Give the position of every malaria parasite.
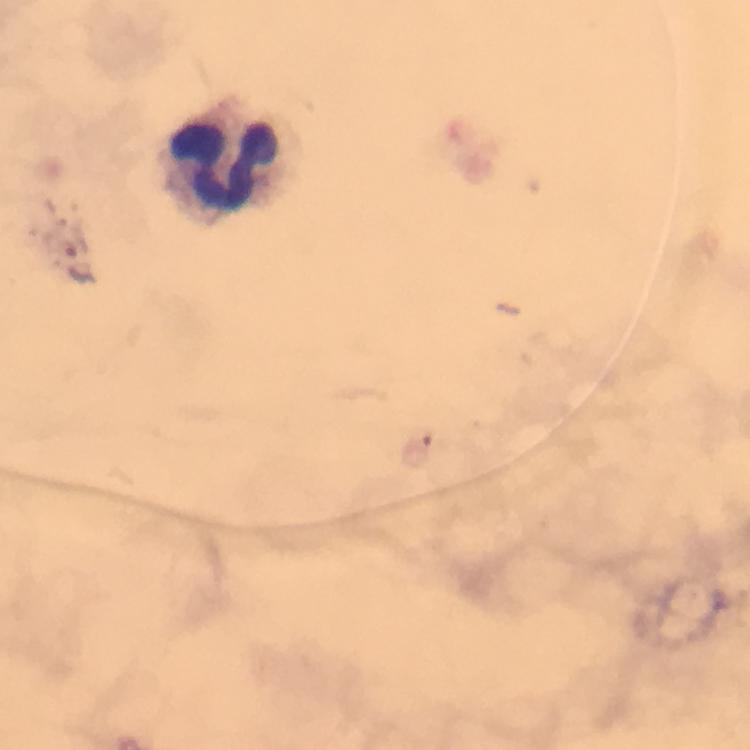

No malaria parasites detected.

Approximate object centers, in pixels from the top-left corner. Leukocyte locations: (x=230, y=160). 100x magnification. Image is 750×750 pixels. Immersion oil was used. Giemsa stain. A crop from one field of view. From a diagnostic examination for malaria. Photographed through the microscope with a smartphone camera. Thick smear.